Assess this cell for malaria.
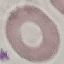
It is uninfected.

Summary:
  - Image type: automatically extracted cell patch, resized to 64 × 64 pixels
  - Stain: Giemsa
  - Capture: smartphone camera at the microscope eyepiece
  - Preparation: thin blood film